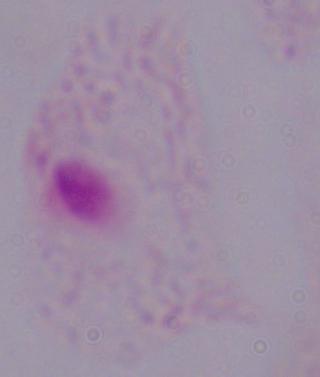
Micrograph. Captured at 1000x magnification. A trichomonad is shown.